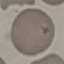

malaria_status: uninfected
stain: Giemsa
capture: smartphone through the microscope eyepiece
preparation: thin blood smear
image_type: cell patch, automatically extracted from a larger field of view and resized to 64 × 64 pixels